Describe the morphology of the red blood cells.
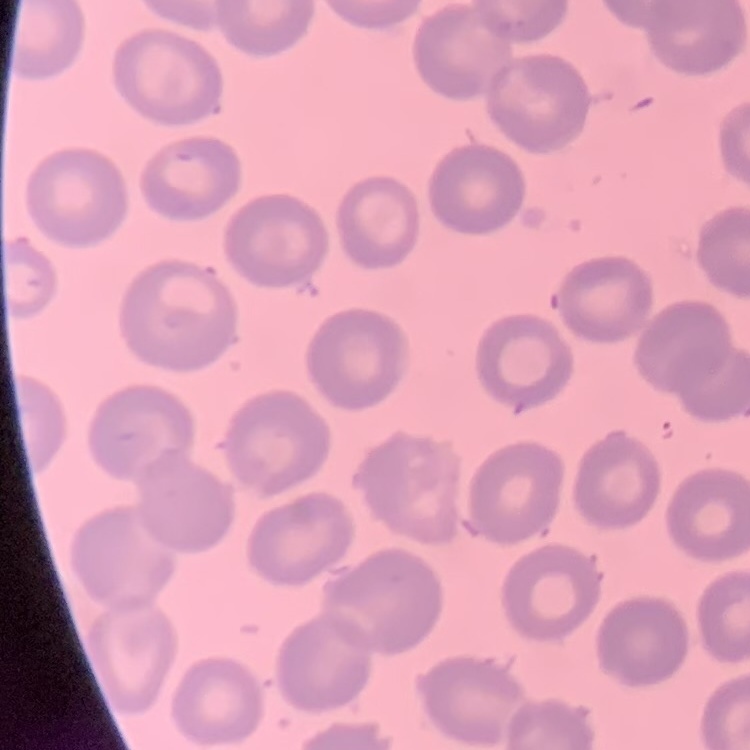

No rouleaux formation.

preparation = thin blood smear
image type = one tile cut from a larger photomicrograph
stain = Field's or Giemsa